Assess this cell for malaria.
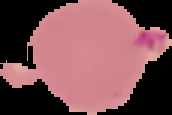
It is parasitized.

From a thin blood smear. Image is 172×115 pixels. The area outside the segmented cell region is set to black.